Comment on the morphology of the red blood cells.
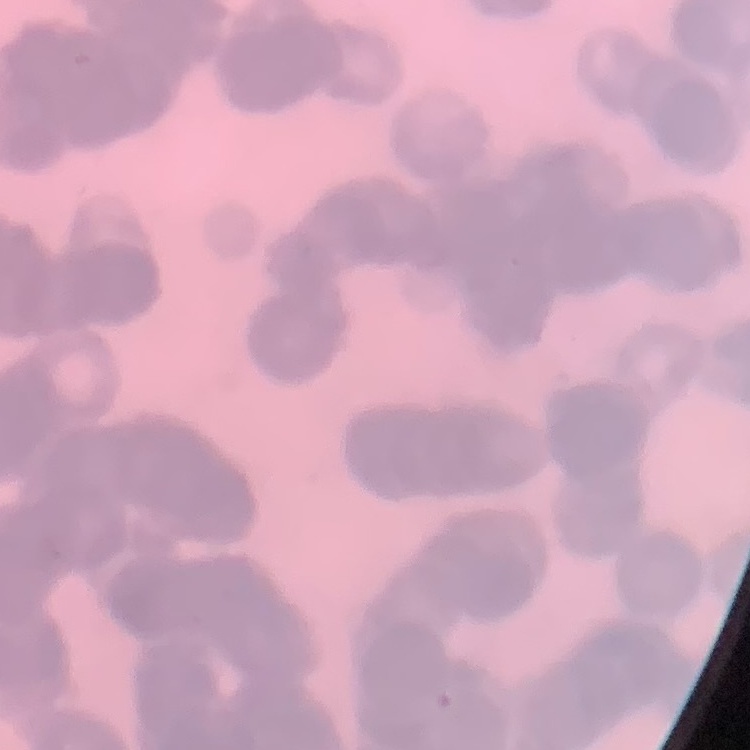

They show rouleaux formation.

Summary:
  - Image type: one tile cut from a larger photomicrograph
  - Preparation: thin blood film
  - Stain: Field's or Giemsa